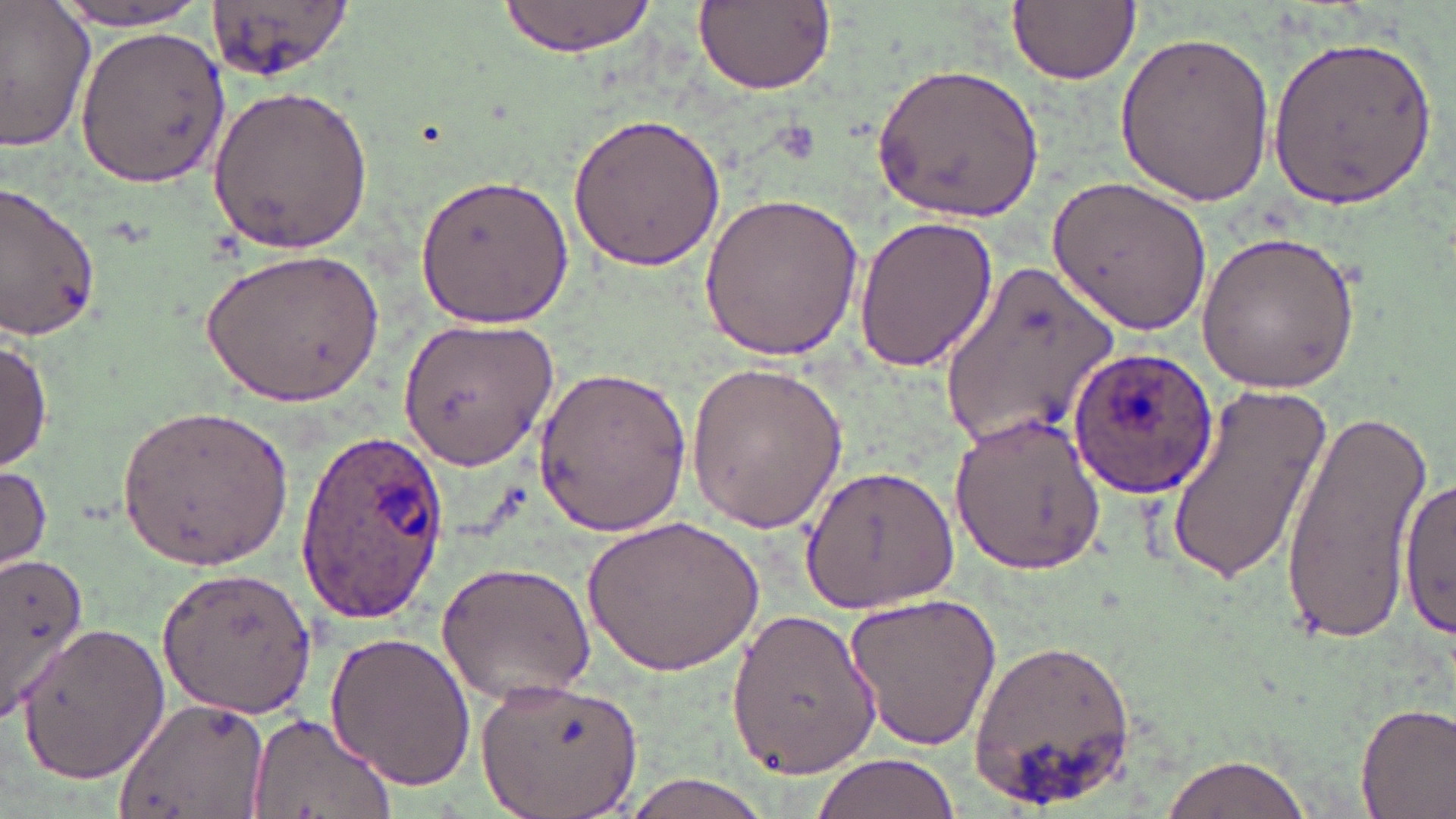

Approximate bounding boxes as (x1,y1)-(x2,y2) corner pairs in pixels. Plasmodium ovale-infected red blood cell locations: (1068,345)-(1220,500), (295,428)-(450,625). Uninfected red blood cell locations: (205,0)-(360,85), (498,0)-(655,57), (1010,0)-(1140,86), (690,1)-(837,96), (41,2)-(220,31), (0,3)-(97,152), (73,24)-(229,187), (1112,28)-(1275,207), (1266,30)-(1438,212), (871,60)-(1047,224), (208,82)-(373,255), (563,112)-(731,274), (1050,171)-(1214,335), (415,172)-(575,332), (0,181)-(103,341), (698,190)-(864,360), (852,212)-(996,374), (1194,228)-(1362,393), (199,247)-(383,408), (938,263)-(1120,447), (395,312)-(562,469), (0,334)-(52,474), (685,357)-(849,537), (533,363)-(693,539), (1162,381)-(1332,587), (117,402)-(294,569), (1281,406)-(1427,644), (952,411)-(1105,577), (0,463)-(52,577), (801,463)-(959,616), (1401,470)-(1456,645), (583,513)-(764,677), (0,551)-(97,722), (437,559)-(597,703), (154,569)-(317,717), (840,588)-(1004,752), (729,605)-(882,780), (16,621)-(169,787), (323,631)-(477,790), (970,635)-(1138,812), (476,673)-(641,819), (114,696)-(266,819), (1355,701)-(1456,819), (244,712)-(393,819), (1155,749)-(1318,819), (808,752)-(962,818), (613,771)-(785,819). Slide-level diagnosis: Plasmodium ovale. Single field of view. Image is 1456×819 pixels. May-Grünwald-Giemsa-stained preparation. Thin blood film. Light microscopy. 1000x magnification.